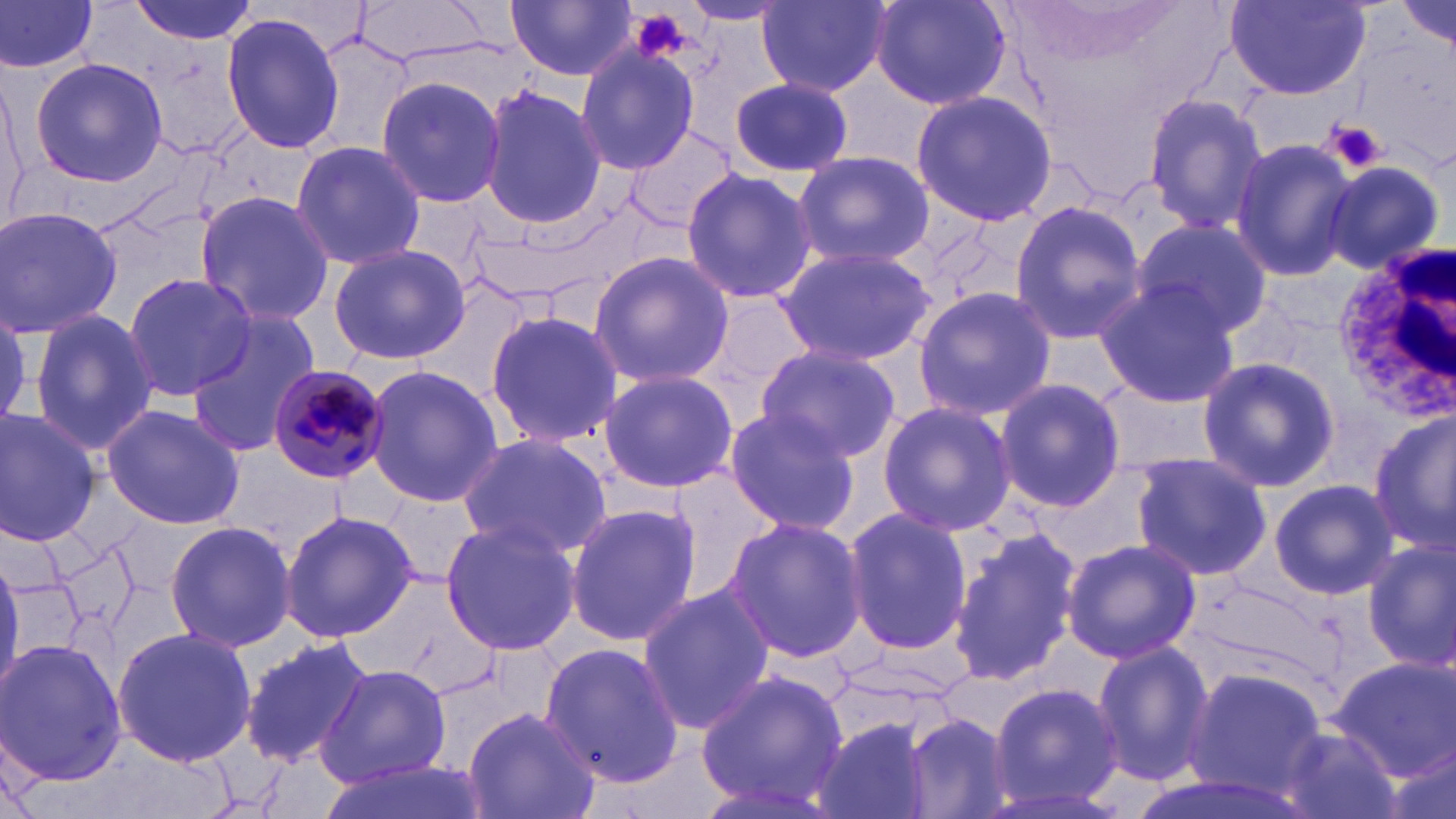
slide-level diagnosis = Plasmodium malariae
platelet locations = approximate bounding boxes as (x1,y1)-(x2,y2) corner pairs in pixels: (631,11)-(694,63), (1325,120)-(1387,174)
white blood cell locations = approximate bounding boxes as (x1,y1)-(x2,y2) corner pairs in pixels: (1333,247)-(1456,414)
stain = May-Grünwald-Giemsa
uninfected red blood cell locations = approximate bounding boxes as (x1,y1)-(x2,y2) corner pairs in pixels: (0,0)-(102,77), (126,0)-(258,47), (757,0)-(892,96), (871,0)-(1011,111), (508,1)-(636,81), (1226,2)-(1371,100), (681,3)-(789,28), (1393,4)-(1455,51), (221,12)-(345,157), (573,43)-(701,176), (29,56)-(167,188), (375,76)-(507,210), (731,78)-(852,177), (478,85)-(607,230), (912,90)-(1060,228), (1142,92)-(1270,234), (1229,137)-(1358,284), (289,139)-(427,271), (792,151)-(934,269), (1322,159)-(1445,275), (680,168)-(817,304), (193,191)-(334,326), (1007,200)-(1145,345), (0,206)-(124,341), (1132,219)-(1275,339), (330,244)-(471,364), (775,244)-(935,365), (587,251)-(735,387), (120,272)-(257,398), (1093,282)-(1242,408), (913,286)-(1059,422), (694,288)-(819,416), (28,309)-(159,456), (484,309)-(625,448), (184,313)-(321,459), (754,345)-(902,463), (1195,354)-(1340,494), (363,365)-(503,507), (597,370)-(738,494), (995,379)-(1128,513), (877,400)-(1018,537), (100,403)-(246,530), (722,407)-(861,534), (0,409)-(100,548), (1370,409)-(1456,554), (456,433)-(612,558), (1126,452)-(1274,583), (660,466)-(780,605), (1269,478)-(1399,600), (564,502)-(703,648), (840,508)-(973,656), (279,510)-(419,645), (722,516)-(867,662), (439,518)-(584,657), (164,520)-(297,653), (947,528)-(1081,689), (1062,537)-(1202,664), (1360,539)-(1456,674), (0,548)-(24,697), (637,585)-(776,732), (109,626)-(259,768), (239,634)-(374,767), (1,638)-(126,786), (540,639)-(684,787), (1091,641)-(1214,785), (1330,658)-(1456,780), (317,663)-(451,787), (1183,666)-(1329,797), (694,667)-(849,812), (985,681)-(1125,812), (463,706)-(599,819), (900,713)-(1015,819), (809,720)-(938,819), (1274,721)-(1405,819), (310,758)-(491,819)
Plasmodium malariae-infected red blood cell locations = approximate bounding boxes as (x1,y1)-(x2,y2) corner pairs in pixels: (268,365)-(390,486)
image size = 1456×819 pixels
field of view = one of a larger specimen
preparation = thin blood film
magnification = 1000x
modality = optical microscopy